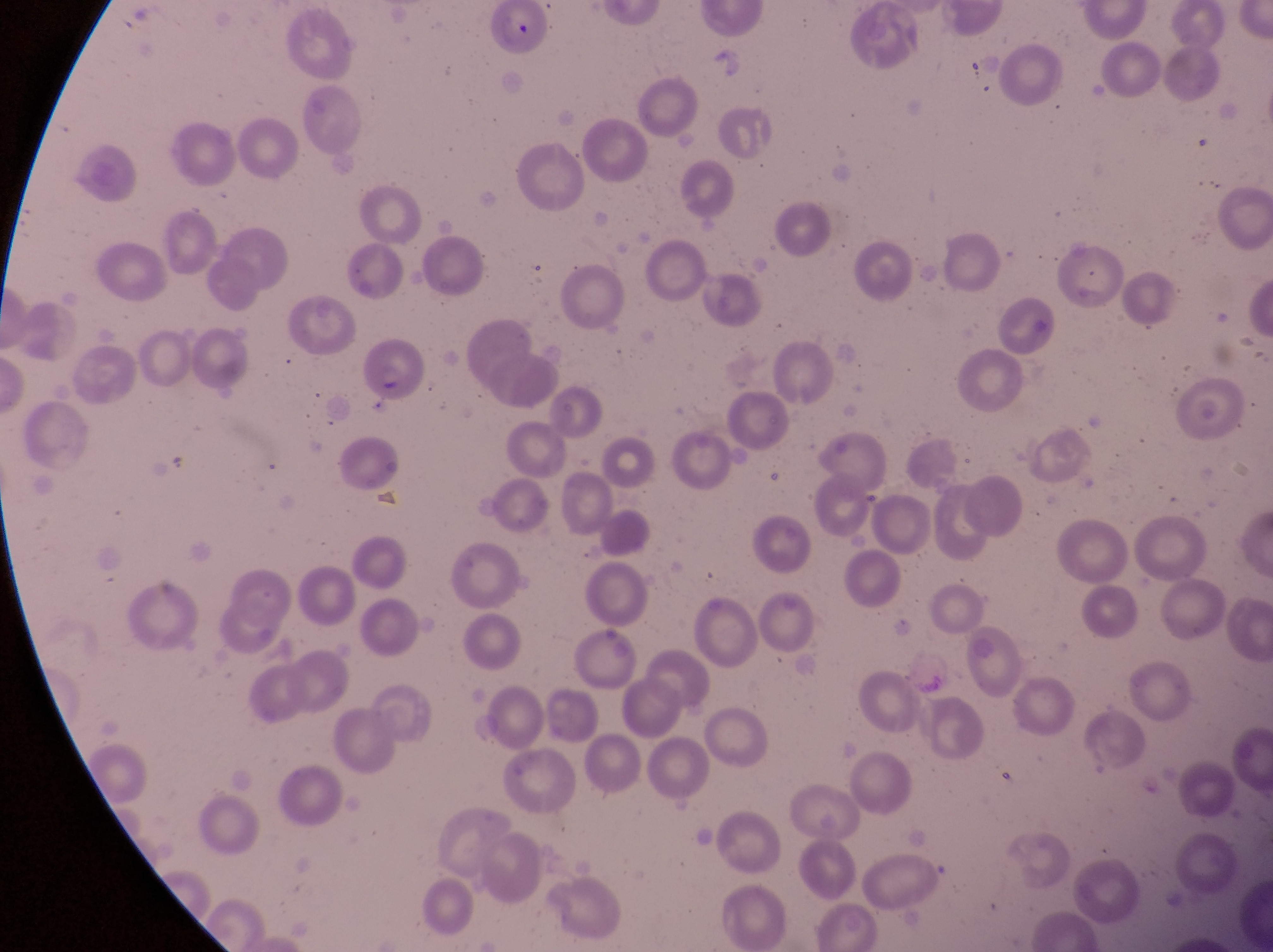

Approximate bounding boxes as (left, top, right, bottom) in pixels.
Summary:
  - Parasitised red blood cell locations: (489, 3, 559, 61), (357, 337, 429, 404)
  - Field of view: single
  - Image size: 1273×952 pixels
  - Magnification: 1000x
  - Capture: smartphone photograph through the eyepiece of an Olympus CX-23 microscope
  - Country: Uganda
  - Preparation: thin blood smear